Report the malaria status of this cell.
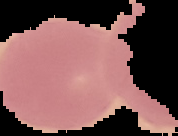
Uninfected.

Cell region segmented out of the field of view; the surrounding area is masked to black. Image is 178×136 pixels. From a thin blood film.